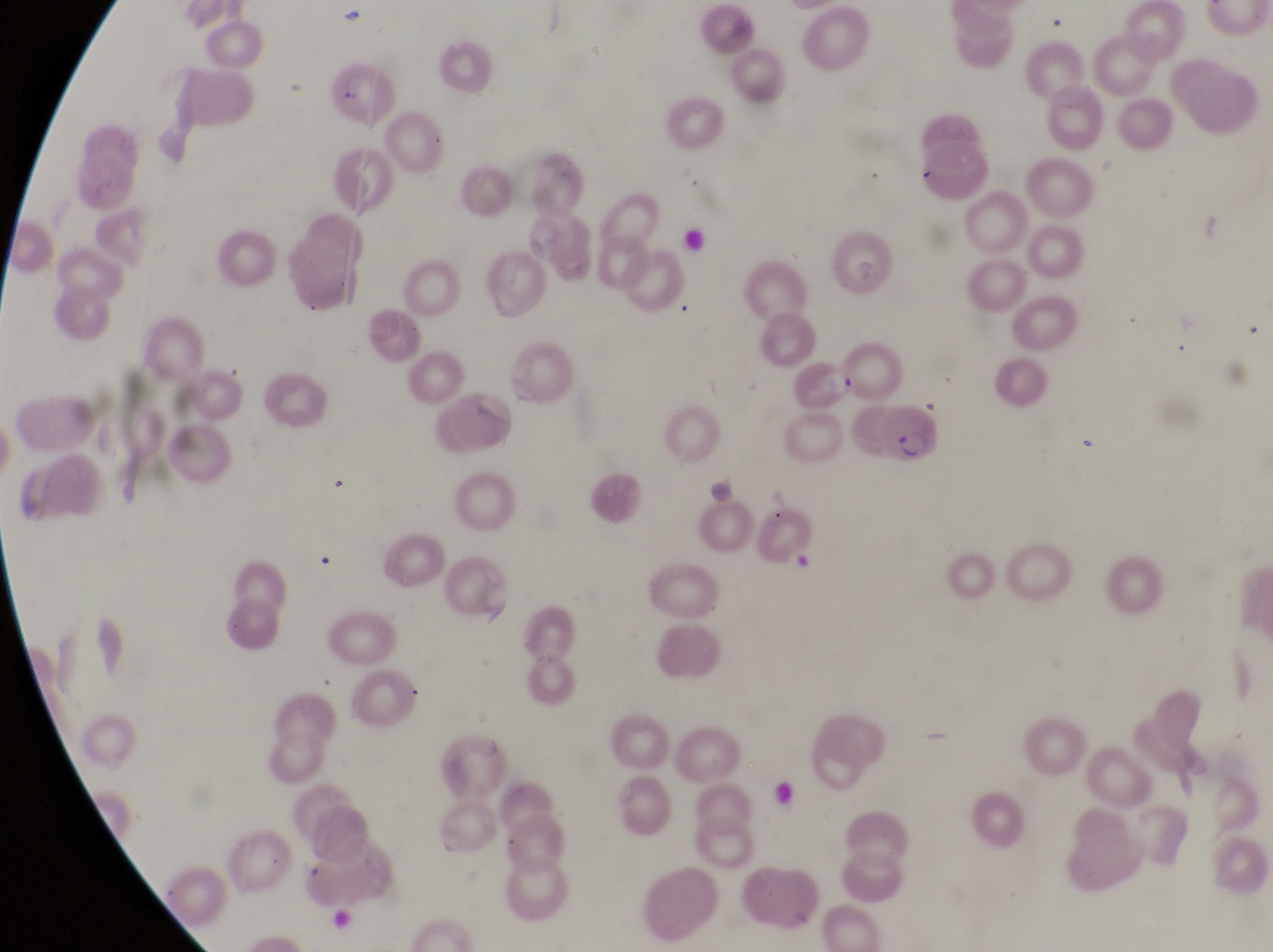
Approximate bounding boxes as left top right bottom in pixels. Artifact (platelet-like body, stain precipitate, or debris) locations: 337 10 365 33; 340 65 367 108. Parasitised red blood cell locations: 874 402 944 467. At a magnification of 1000x. One field of view. Captured by a smartphone held over the eyepiece of an Olympus CX-23 microscope. Thin blood film. Image is 1273×952 pixels. Sample from Uganda.